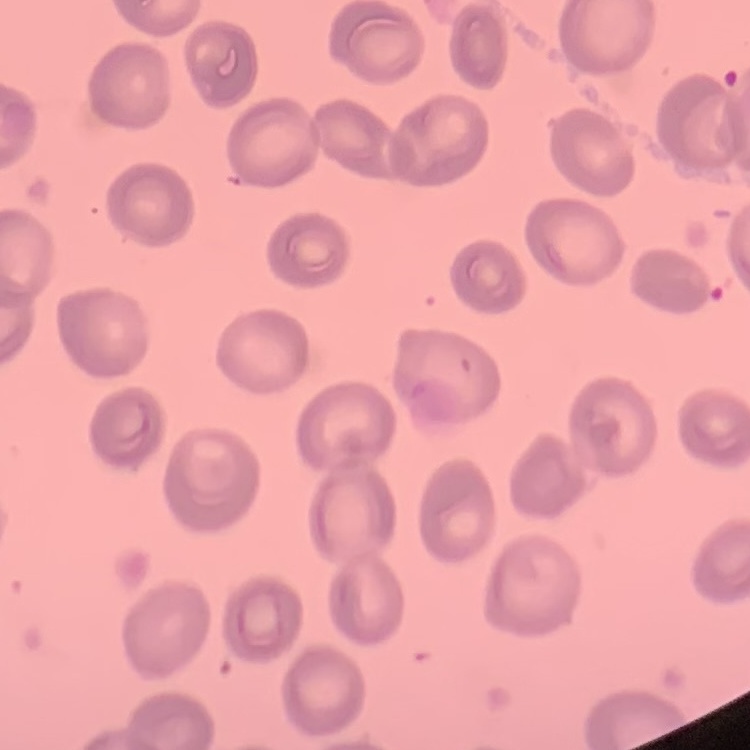

The erythrocytes show no rouleaux formation. Thin peripheral smear. Square crop of a larger photomicrograph. Stained with either Field's or Giemsa.